Give the position of every Plasmodium parasite.
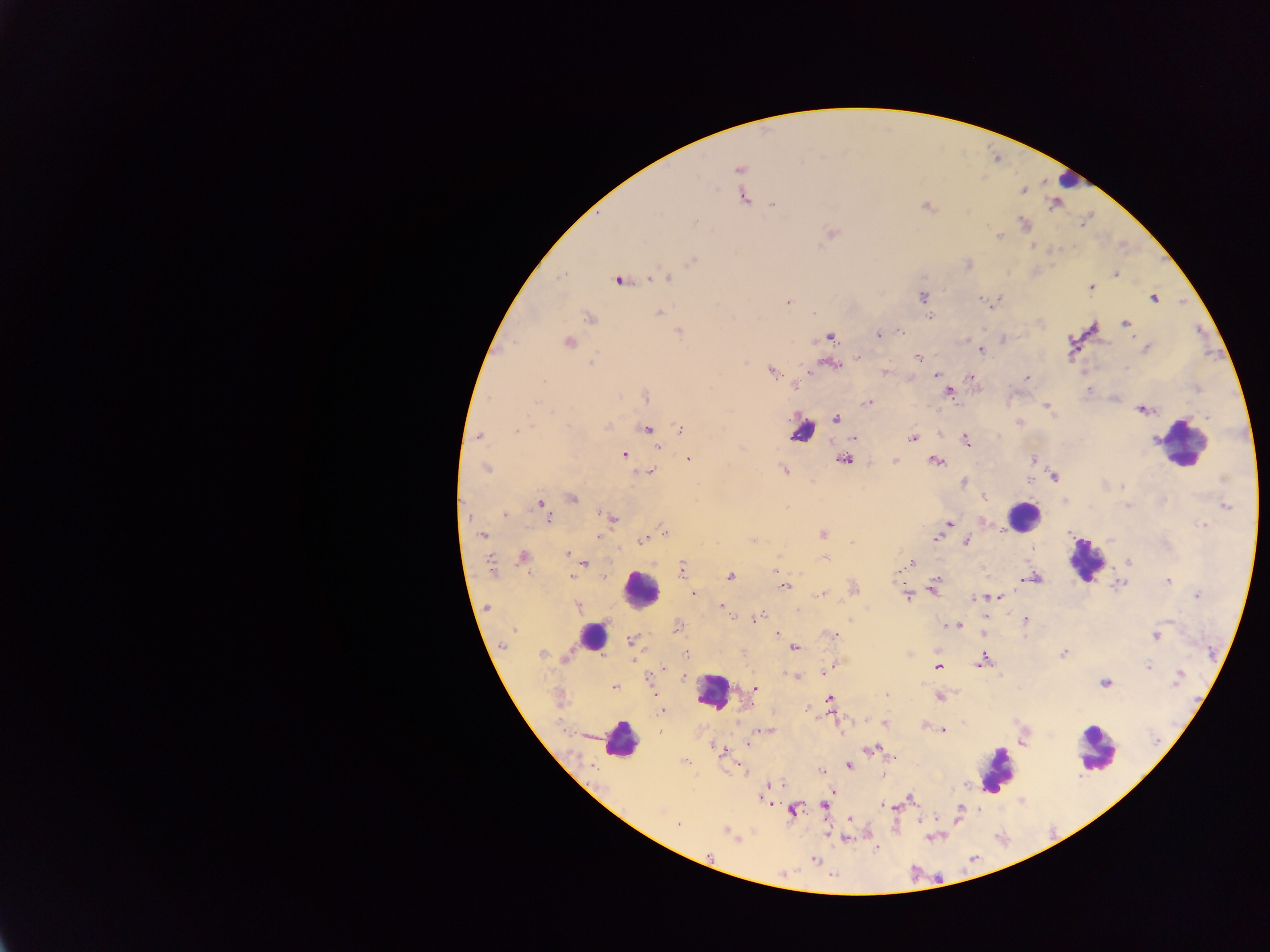

Approximate centers as [x, y] in pixels.
Plasmodium parasites: [739, 169], [741, 182], [1021, 190], [743, 197], [772, 202], [1055, 202], [925, 205], [695, 221], [1025, 223], [831, 233], [998, 235], [1032, 245], [692, 260], [968, 264], [1115, 274], [666, 276], [647, 279], [618, 280], [1091, 288], [922, 296], [981, 298], [1153, 298], [992, 302], [787, 303], [659, 312], [931, 315], [589, 318], [1125, 324], [901, 330], [678, 331], [878, 334], [829, 335], [1003, 339], [567, 342], [1146, 349], [980, 350], [917, 358], [830, 363], [772, 372], [884, 372], [935, 374], [908, 377], [972, 377], [1026, 378], [948, 391], [646, 396], [868, 403], [1047, 406], [1142, 409], [836, 418], [1019, 422], [681, 427], [648, 430], [517, 431], [939, 433], [477, 435], [853, 438], [912, 439], [966, 440], [658, 446], [624, 454], [688, 458], [844, 459], [1033, 459], [935, 460], [894, 461], [486, 468], [783, 469], [649, 471], [1053, 475], [1029, 479], [963, 482], [1123, 486], [982, 496], [571, 498], [1065, 501], [540, 504], [1225, 505], [545, 507], [504, 513], [611, 517], [548, 518], [981, 522], [949, 523], [1203, 526], [663, 532], [822, 533], [482, 534], [598, 536], [937, 537], [642, 539], [753, 540], [966, 541], [851, 542], [567, 553], [523, 557], [571, 557], [825, 558], [1129, 561], [583, 563], [909, 564], [682, 571], [729, 575], [572, 576], [603, 576], [1033, 577], [1168, 581], [784, 584], [1119, 584], [934, 587], [853, 588], [693, 593], [822, 594], [907, 596], [997, 596], [1197, 596], [975, 598], [576, 606], [719, 606], [487, 607], [985, 617], [755, 619], [1025, 620], [945, 625], [957, 625], [678, 627], [776, 633], [832, 634], [983, 634], [1155, 635], [632, 640], [503, 644], [794, 647], [686, 653], [1064, 653], [542, 655], [566, 658], [632, 661], [981, 661], [833, 666], [938, 667], [1147, 667], [663, 670], [825, 671], [796, 677], [1179, 677], [649, 681], [1105, 683], [614, 687], [755, 688], [886, 694], [940, 696], [830, 698], [662, 710], [806, 710], [866, 720], [885, 723], [924, 724], [768, 730], [943, 730], [749, 743], [872, 749], [721, 750], [725, 755], [849, 765], [742, 769], [821, 772], [883, 773], [768, 788], [832, 792], [910, 799], [768, 802], [823, 805], [886, 806], [894, 806], [793, 811], [849, 820], [678, 824], [728, 832], [828, 832], [846, 837], [877, 846], [708, 856], [813, 860].

Summary:
  - Leukocyte locations: [1068, 179], [802, 429], [1184, 443], [1023, 516], [1086, 560], [641, 590], [592, 635], [711, 691], [620, 740], [1097, 747], [996, 769]
  - Image size: 1270×952 pixels
  - Preparation: thick blood film
  - Country: Ghana
  - Capture: mobile-phone photograph through a microscope
  - Field of view: single